Assess this cell for malaria.
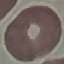

It is uninfected.

Giemsa-stained preparation. Acquired by smartphone through the microscope eyepiece. Thin blood film. Cell patch, automatically extracted from a larger field of view and resized to 64 × 64 pixels.